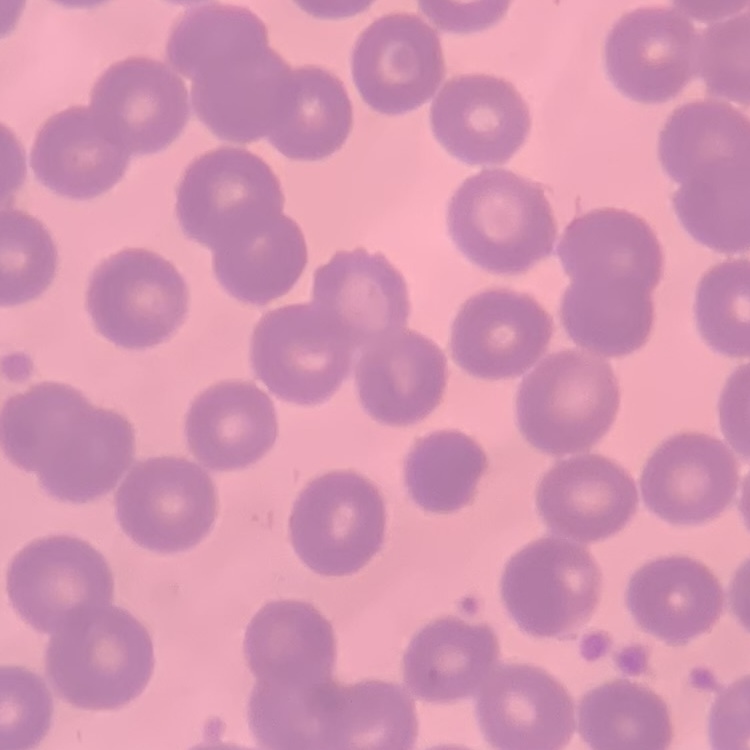

The red blood cells show no rouleaux formation. Square crop of a larger photomicrograph. Thin blood film. Stained with either Field's or Giemsa.